Assess this cell for malaria.
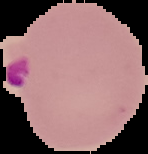

Parasitized.

Image is 148×154 pixels. Segmented cell region on a black background. From a thin blood smear.